Assess this cell for malaria.
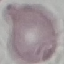
It is uninfected.

capture: smartphone camera at the microscope eyepiece
preparation: thin blood film
image_type: automatically extracted cell patch, resized to 64 × 64 pixels
stain: Giemsa